Locate every blood parasite and identify its species.
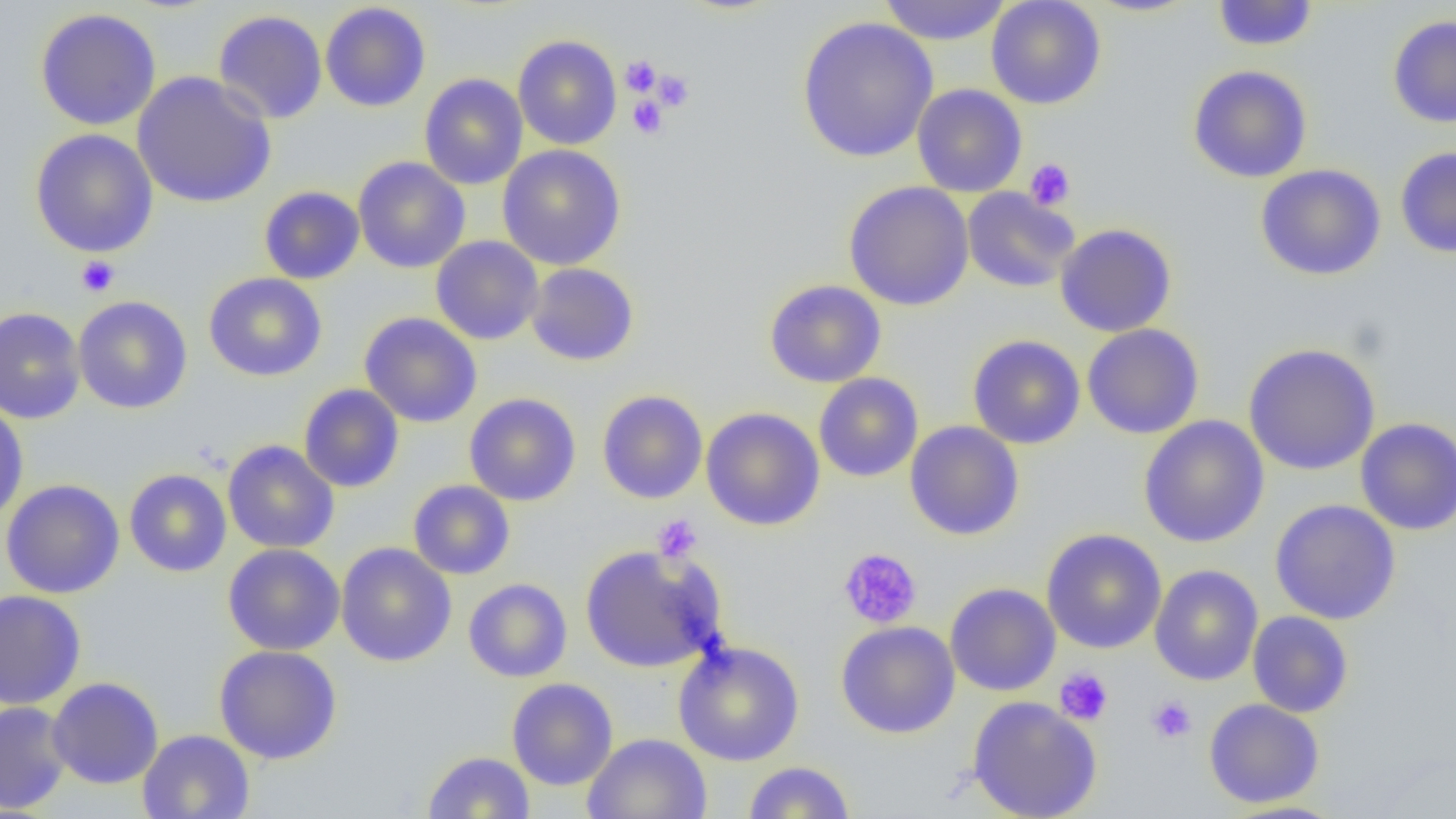

No blood parasites seen.

{
  "slide_level_diagnosis": "no evidence of blood parasites",
  "modality": "light microscopy",
  "image_size": "1456×819 pixels",
  "platelet_locations": "approximate bounding boxes as named x1/y1/x2/y2 corners in pixels: (x1=620, y1=56, x2=662, y2=96), (x1=652, y1=69, x2=694, y2=112), (x1=628, y1=95, x2=668, y2=139), (x1=1024, y1=158, x2=1076, y2=210), (x1=77, y1=256, x2=120, y2=297), (x1=653, y1=514, x2=702, y2=562), (x1=839, y1=547, x2=922, y2=629), (x1=1054, y1=668, x2=1113, y2=726), (x1=1146, y1=696, x2=1197, y2=744)",
  "preparation": "thin blood smear",
  "magnification": "1000x",
  "field_of_view": "one of a larger specimen",
  "uninfected_red_blood_cell_locations": "approximate bounding boxes as named x1/y1/x2/y2 corners in pixels: (x1=877, y1=0, x2=1012, y2=46), (x1=986, y1=0, x2=1106, y2=109), (x1=1084, y1=0, x2=1203, y2=17), (x1=1211, y1=1, x2=1319, y2=51), (x1=320, y1=2, x2=431, y2=112), (x1=35, y1=8, x2=162, y2=131), (x1=213, y1=10, x2=327, y2=124), (x1=1387, y1=15, x2=1456, y2=128), (x1=797, y1=16, x2=938, y2=163), (x1=513, y1=35, x2=622, y2=150), (x1=1187, y1=65, x2=1313, y2=183), (x1=132, y1=71, x2=277, y2=208), (x1=419, y1=73, x2=528, y2=190), (x1=912, y1=84, x2=1027, y2=197), (x1=30, y1=128, x2=158, y2=257), (x1=497, y1=145, x2=626, y2=270), (x1=1395, y1=146, x2=1456, y2=258), (x1=353, y1=157, x2=470, y2=274), (x1=1255, y1=164, x2=1387, y2=281), (x1=844, y1=181, x2=974, y2=311), (x1=258, y1=186, x2=365, y2=284), (x1=961, y1=187, x2=1080, y2=293), (x1=1055, y1=224, x2=1177, y2=337), (x1=430, y1=236, x2=544, y2=345), (x1=526, y1=262, x2=639, y2=366), (x1=203, y1=272, x2=328, y2=382), (x1=764, y1=279, x2=886, y2=387), (x1=72, y1=296, x2=192, y2=414), (x1=0, y1=307, x2=86, y2=424), (x1=359, y1=312, x2=482, y2=428), (x1=1082, y1=323, x2=1205, y2=440), (x1=967, y1=335, x2=1085, y2=449), (x1=1243, y1=343, x2=1381, y2=475), (x1=814, y1=373, x2=923, y2=482), (x1=298, y1=384, x2=405, y2=492), (x1=597, y1=390, x2=708, y2=504), (x1=464, y1=393, x2=581, y2=506), (x1=0, y1=400, x2=29, y2=525), (x1=701, y1=407, x2=825, y2=531), (x1=1138, y1=415, x2=1269, y2=548), (x1=1355, y1=417, x2=1456, y2=535), (x1=904, y1=421, x2=1024, y2=541), (x1=223, y1=440, x2=339, y2=553), (x1=124, y1=469, x2=232, y2=577), (x1=1, y1=479, x2=124, y2=598), (x1=408, y1=480, x2=515, y2=579), (x1=1270, y1=499, x2=1401, y2=625), (x1=1041, y1=528, x2=1167, y2=654), (x1=336, y1=542, x2=457, y2=667), (x1=222, y1=543, x2=345, y2=656), (x1=579, y1=544, x2=727, y2=673), (x1=1149, y1=564, x2=1263, y2=686), (x1=463, y1=578, x2=572, y2=682), (x1=945, y1=582, x2=1061, y2=696), (x1=0, y1=589, x2=86, y2=710), (x1=1247, y1=611, x2=1354, y2=718), (x1=836, y1=621, x2=960, y2=739), (x1=672, y1=640, x2=805, y2=766), (x1=213, y1=645, x2=342, y2=764), (x1=47, y1=677, x2=164, y2=789), (x1=506, y1=677, x2=618, y2=790), (x1=967, y1=696, x2=1103, y2=819), (x1=1204, y1=698, x2=1325, y2=808), (x1=0, y1=701, x2=73, y2=814), (x1=138, y1=729, x2=255, y2=819), (x1=582, y1=733, x2=713, y2=819), (x1=422, y1=751, x2=535, y2=818), (x1=742, y1=761, x2=856, y2=818), (x1=1217, y1=799, x2=1350, y2=818)"
}